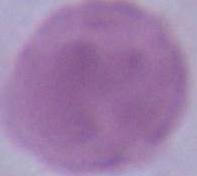
Summary:
  - Magnification: 1000x
  - Modality: micrograph
  - Identification: red blood cell